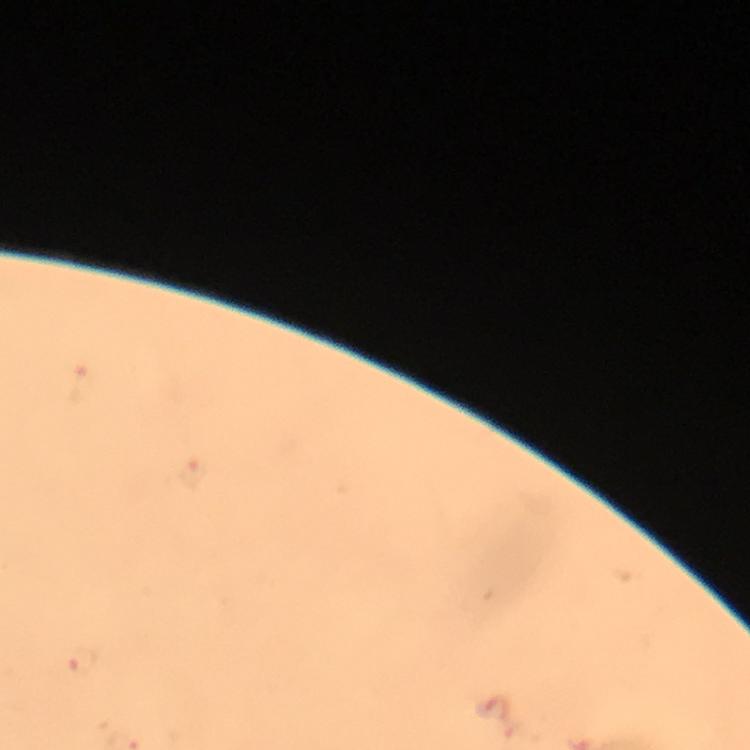 Approximate centers as {x, y} in pixels. Malaria parasite locations: {85, 662}. A crop from one field of view. From a diagnostic examination for malaria. Immersion oil applied. Photographed through the microscope with a smartphone camera. Giemsa stain. At 100x magnification. Image is 750×750 pixels. Thick blood film.